Assess this cell for malaria.
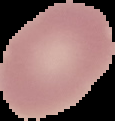

It is uninfected.

image size = 115×121 pixels
image type = cell region segmented out of the field of view; surrounding area masked to black
preparation = thin blood smear